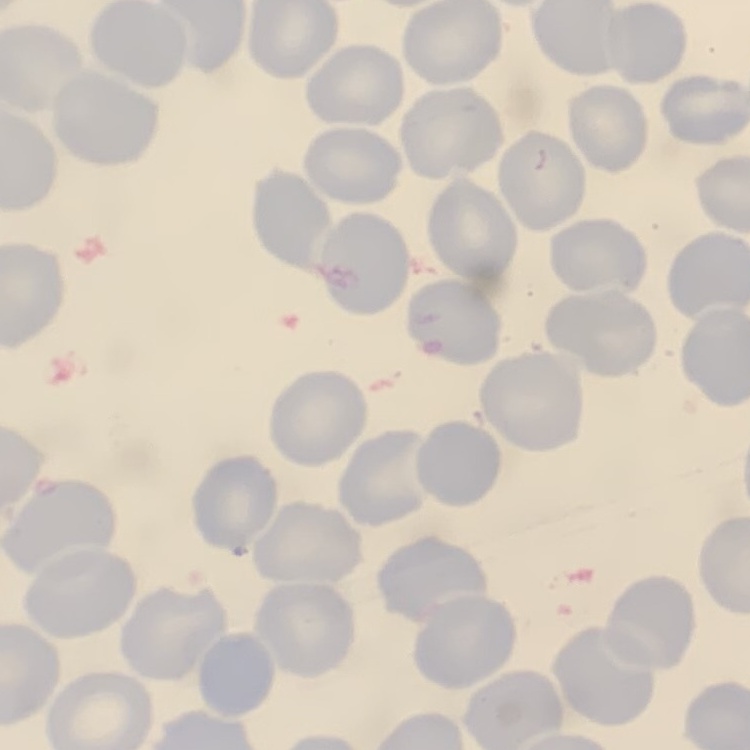
Summary:
  - Red blood cell morphology: no rouleaux formation
  - Image type: one tile cut from a larger photomicrograph
  - Stain: Field's or Giemsa
  - Preparation: thin blood smear